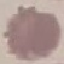

result: no malaria parasites seen
capture: smartphone camera at the microscope eyepiece
image_type: cell patch, automatically extracted from a larger field of view and resized to 64 × 64 pixels
stain: Giemsa
preparation: thin blood smear